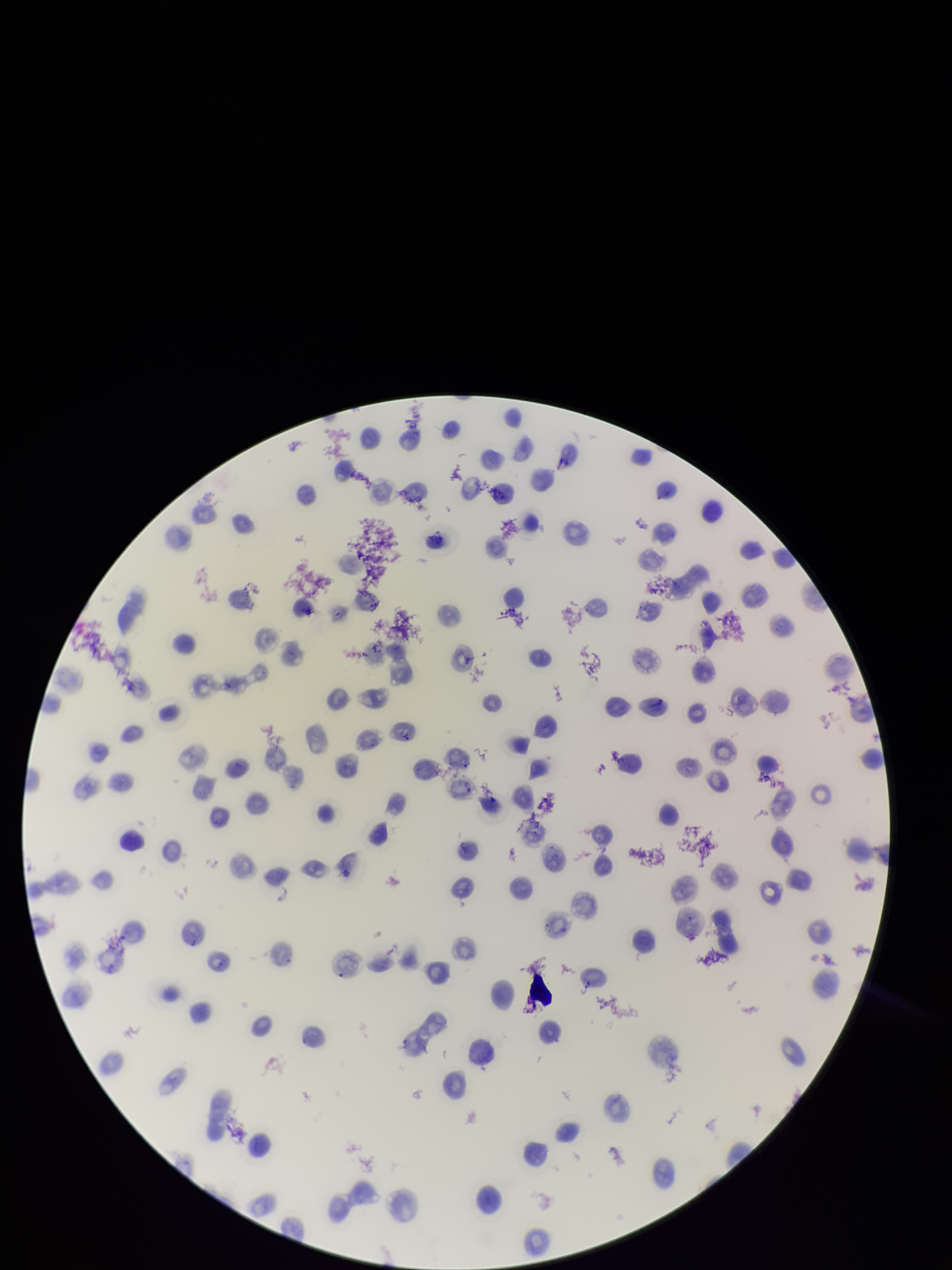
{
  "preparation": "thin smear",
  "stain": "Giemsa",
  "parasitized_red_blood_cells": "none detected",
  "field_of_view": "single",
  "parasitized_red_blood_cell_count": 0,
  "species_reported_for_this_patient": "Plasmodium vivax",
  "red_blood_cell_count": 115,
  "capture": "smartphone photograph through the microscope eyepiece",
  "patient_malaria_status": "infected",
  "image_size": "952×1270 pixels"
}